Name the blood parasite species.
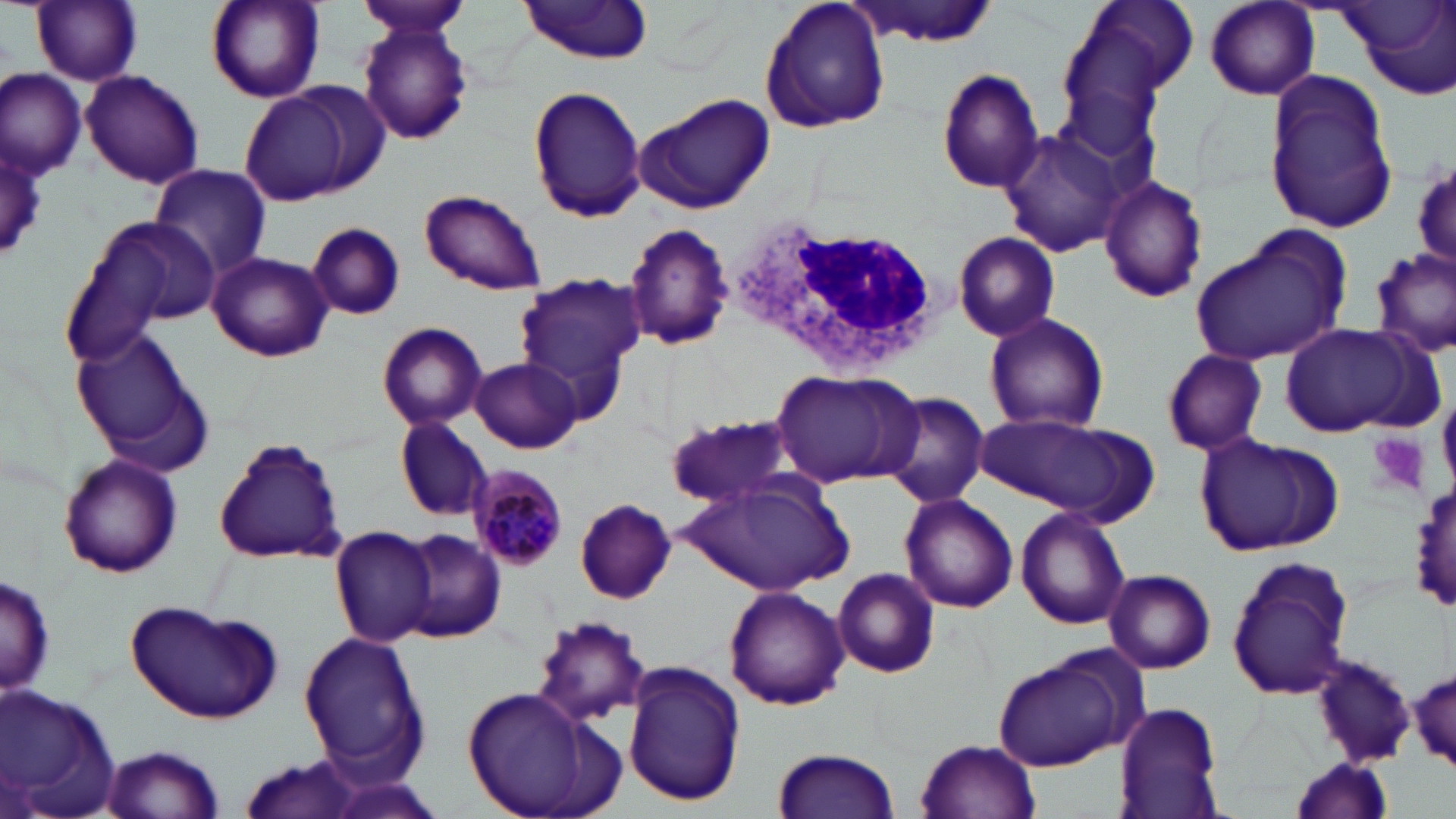
Plasmodium malariae.

Summary:
  - Coordinate format: approximate bounding boxes as [x1, y1, x2, y2] in pixels
  - Platelet locations: [1367, 432, 1428, 496]
  - Plasmodium malariae-infected red blood cell locations: [467, 463, 568, 573]
  - Uninfected red blood cell locations: [28, 0, 145, 86], [356, 0, 472, 38], [760, 0, 890, 135], [848, 0, 1000, 49], [1074, 0, 1200, 102], [1345, 0, 1456, 99], [203, 1, 325, 104], [516, 1, 657, 62], [1204, 1, 1322, 102], [358, 20, 475, 147], [936, 67, 1045, 193], [2, 68, 86, 182], [80, 68, 204, 188], [1264, 74, 1397, 236], [240, 84, 365, 204], [527, 85, 647, 223], [638, 95, 775, 215], [1000, 127, 1123, 257], [1410, 154, 1455, 273], [149, 163, 271, 277], [1099, 176, 1208, 304], [417, 188, 546, 296], [60, 212, 216, 365], [623, 221, 735, 353], [308, 223, 406, 321], [1190, 229, 1352, 368], [951, 231, 1061, 344], [1371, 247, 1455, 361], [208, 251, 333, 362], [512, 272, 643, 395], [985, 313, 1109, 434], [377, 321, 488, 431], [1280, 322, 1425, 435], [72, 327, 206, 457], [1161, 348, 1271, 456], [469, 357, 582, 453], [772, 368, 921, 488], [880, 392, 991, 510], [973, 412, 1156, 522], [665, 413, 805, 512], [395, 417, 492, 521], [1195, 433, 1333, 554], [215, 437, 347, 564], [57, 454, 183, 579], [681, 475, 856, 598], [1411, 479, 1456, 613], [899, 494, 1019, 614], [575, 498, 677, 603], [1015, 504, 1130, 631], [330, 524, 438, 646], [399, 529, 507, 643], [1226, 556, 1355, 699], [833, 566, 942, 678], [1103, 569, 1216, 675], [1, 571, 54, 702], [725, 585, 848, 710], [125, 601, 284, 725], [531, 614, 656, 728], [299, 631, 429, 775], [989, 652, 1134, 771], [1310, 654, 1417, 768], [1395, 659, 1456, 773], [624, 663, 745, 808], [2, 684, 122, 819], [459, 686, 612, 819], [1115, 701, 1226, 818], [915, 737, 1043, 819], [97, 745, 227, 818], [772, 746, 902, 819], [234, 753, 368, 819], [1287, 755, 1398, 819]
  - White blood cell locations: [728, 218, 951, 376]
  - Field of view: one of a larger specimen
  - Modality: light microscopy
  - Image size: 1456×819 pixels
  - Stain: May-Grünwald-Giemsa
  - Magnification: 1000x
  - Preparation: thin blood film